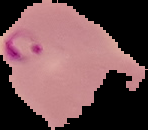
image_type: cell region segmented out of the field of view; surrounding area masked to black
image_size: 148×130 pixels
result: malaria parasites detected
preparation: thin blood film